Locate and identify every blood parasite.
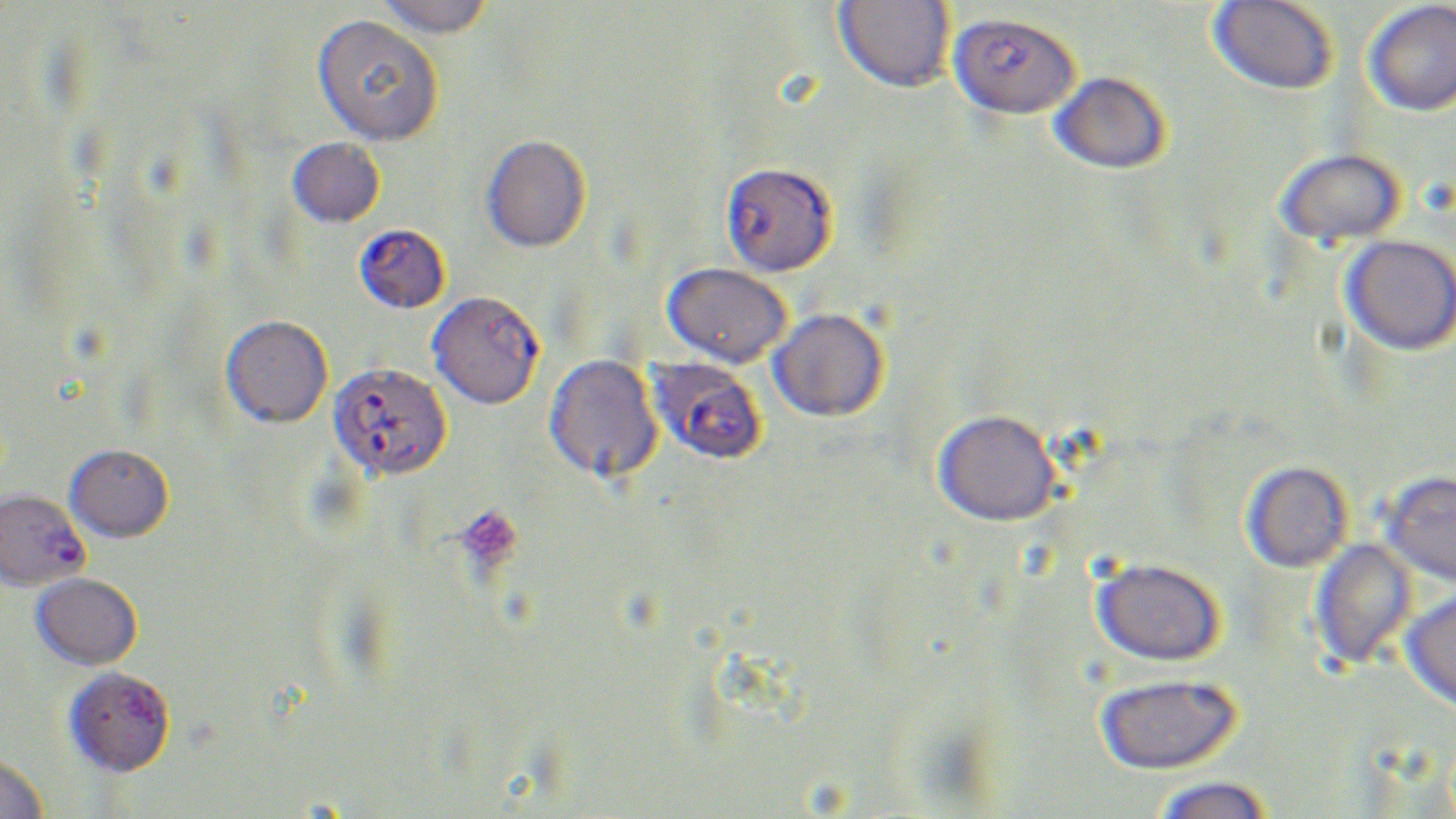
Approximate bounding boxes as (x1,y1)-(x2,y2) corner pairs in pixels.
Plasmodium falciparum-infected red blood cells: (949,12)-(1080,119), (720,161)-(837,276), (354,224)-(450,314), (427,291)-(544,409), (647,357)-(766,465), (328,362)-(452,480), (0,488)-(89,591).
No Plasmodium ovale, Plasmodium malariae, Plasmodium vivax, Babesia divergens, or Trypanosoma brucei observed.

Uninfected red blood cell locations: (374,0)-(493,39), (833,0)-(956,92), (1208,0)-(1338,96), (1362,1)-(1456,117), (311,14)-(443,146), (1050,71)-(1171,174), (481,134)-(590,252), (287,137)-(385,228), (1276,148)-(1406,246), (1341,234)-(1456,356), (662,262)-(792,368), (768,307)-(889,421), (220,314)-(333,428), (543,354)-(664,483), (933,409)-(1061,526), (65,444)-(174,542), (1241,461)-(1353,572), (1380,470)-(1456,587), (1309,537)-(1419,672), (1091,557)-(1225,667), (31,572)-(142,670), (1400,588)-(1456,712), (64,667)-(175,777), (1095,673)-(1243,775), (0,755)-(48,819), (1151,776)-(1276,819). Platelet locations: (454,504)-(524,574). Slide-level diagnosis: Plasmodium falciparum. Captured at 1000x magnification. Image is 1456×819 pixels. May-Grünwald-Giemsa-stained preparation. Thin blood smear. Optical microscopy. One field of a larger specimen.